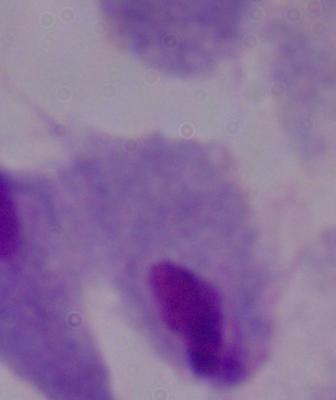

Summary:
  - Magnification: 1000x
  - Identification: trichomonad
  - Modality: photomicrograph